Classify this cell by malaria status.
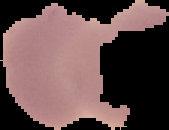

Uninfected.

Image is 169×130 pixels. From a thin blood smear. Cell region segmented out of the field of view; the surrounding area is masked to black.